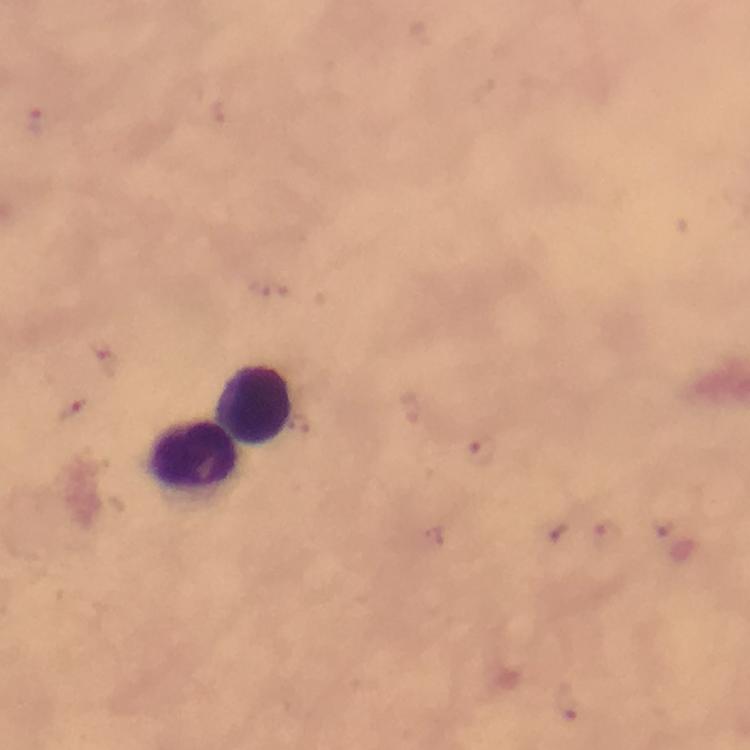 Approximate centers as [x, y] in pixels. Leukocyte locations: [258, 405], [197, 453]. Malaria parasite locations: [40, 123], [75, 407], [483, 451], [604, 538], [567, 703]. Giemsa stain. Thick smear. From a diagnostic examination for malaria. At 100x magnification. Immersion oil applied. Image is 750×750 pixels. Cropped region of a single field of view. Photographed through the microscope with a smartphone camera.